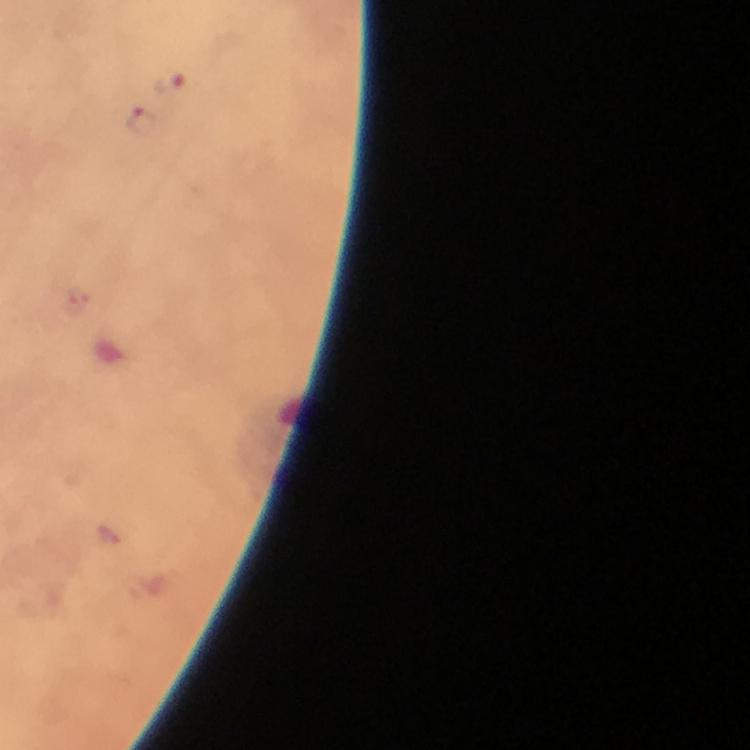 Approximate object centers, in pixels from the top-left corner. Plasmodium parasite locations: (x=173, y=84), (x=140, y=120). Immersion oil was used. At 100x magnification. Photographed through the microscope with a smartphone camera. Cropped region of a single field of view. From a malaria diagnostic workup. Giemsa stain. Thick blood smear. Image is 750×750 pixels.